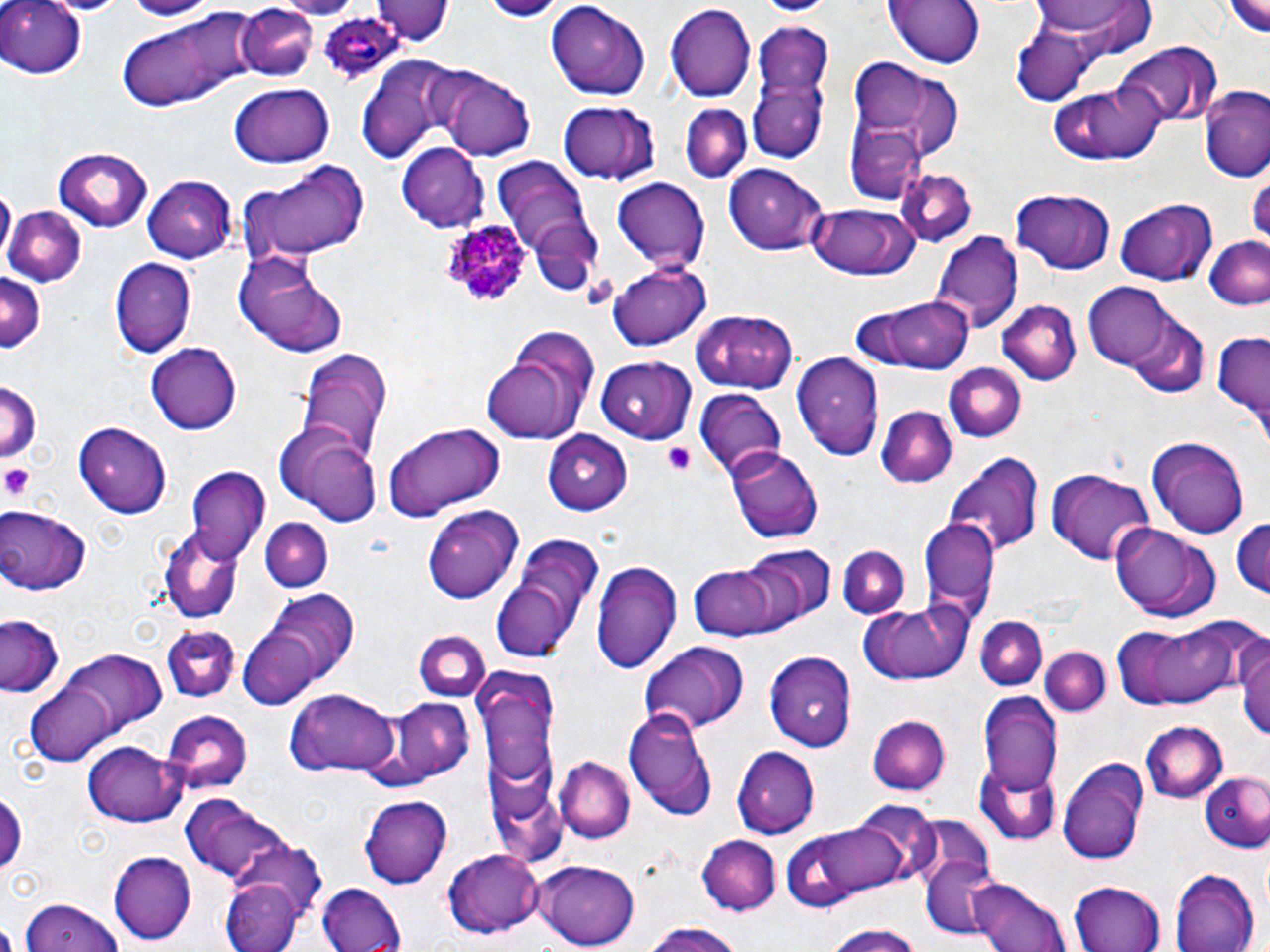

Summary:
  - Coordinate format: approximate bounding boxes as named x1/y1/x2/y2 corners in pixels
  - Platelet locations: (x1=664, y1=444, x2=696, y2=476), (x1=1, y1=464, x2=38, y2=502)
  - Plasmodium ovale-infected red blood cell locations: (x1=319, y1=8, x2=403, y2=81), (x1=440, y1=218, x2=529, y2=307)
  - Uninfected red blood cell locations: (x1=122, y1=0, x2=215, y2=20), (x1=281, y1=0, x2=357, y2=16), (x1=378, y1=0, x2=452, y2=46), (x1=757, y1=0, x2=835, y2=17), (x1=887, y1=0, x2=983, y2=68), (x1=1222, y1=0, x2=1270, y2=38), (x1=0, y1=1, x2=90, y2=79), (x1=46, y1=1, x2=129, y2=15), (x1=1030, y1=1, x2=1155, y2=49), (x1=543, y1=2, x2=650, y2=102), (x1=665, y1=3, x2=754, y2=102), (x1=234, y1=5, x2=321, y2=81), (x1=119, y1=14, x2=263, y2=111), (x1=747, y1=19, x2=833, y2=164), (x1=1009, y1=28, x2=1097, y2=105), (x1=1114, y1=43, x2=1221, y2=126), (x1=354, y1=55, x2=466, y2=164), (x1=849, y1=59, x2=967, y2=160), (x1=442, y1=71, x2=534, y2=161), (x1=1052, y1=80, x2=1168, y2=166), (x1=229, y1=83, x2=335, y2=169), (x1=1202, y1=91, x2=1270, y2=181), (x1=555, y1=101, x2=663, y2=187), (x1=680, y1=104, x2=751, y2=183), (x1=847, y1=125, x2=923, y2=204), (x1=396, y1=141, x2=489, y2=229), (x1=53, y1=146, x2=153, y2=230), (x1=493, y1=157, x2=597, y2=268), (x1=239, y1=160, x2=371, y2=263), (x1=726, y1=165, x2=830, y2=257), (x1=896, y1=169, x2=975, y2=247), (x1=143, y1=176, x2=238, y2=261), (x1=610, y1=177, x2=709, y2=275), (x1=0, y1=185, x2=14, y2=264), (x1=1012, y1=191, x2=1115, y2=274), (x1=1117, y1=200, x2=1216, y2=283), (x1=807, y1=203, x2=920, y2=282), (x1=4, y1=205, x2=84, y2=289), (x1=528, y1=221, x2=601, y2=296), (x1=927, y1=230, x2=1023, y2=334), (x1=1203, y1=235, x2=1270, y2=314), (x1=232, y1=250, x2=350, y2=359), (x1=108, y1=256, x2=196, y2=359), (x1=606, y1=262, x2=712, y2=351), (x1=0, y1=274, x2=43, y2=355), (x1=1084, y1=283, x2=1176, y2=370), (x1=846, y1=295, x2=976, y2=376), (x1=996, y1=300, x2=1080, y2=387), (x1=695, y1=308, x2=800, y2=393), (x1=1127, y1=310, x2=1209, y2=398), (x1=1210, y1=331, x2=1269, y2=433), (x1=146, y1=343, x2=242, y2=434), (x1=292, y1=348, x2=396, y2=464), (x1=483, y1=348, x2=591, y2=444), (x1=789, y1=353, x2=885, y2=460), (x1=596, y1=356, x2=694, y2=443), (x1=945, y1=363, x2=1027, y2=444), (x1=0, y1=379, x2=41, y2=468), (x1=695, y1=390, x2=785, y2=484), (x1=875, y1=407, x2=955, y2=488), (x1=383, y1=422, x2=505, y2=519), (x1=73, y1=423, x2=170, y2=516), (x1=274, y1=425, x2=382, y2=527), (x1=545, y1=431, x2=632, y2=515), (x1=1147, y1=435, x2=1249, y2=541), (x1=727, y1=449, x2=822, y2=543), (x1=943, y1=452, x2=1042, y2=556), (x1=186, y1=468, x2=271, y2=567), (x1=1046, y1=469, x2=1153, y2=564), (x1=421, y1=505, x2=525, y2=604), (x1=0, y1=506, x2=91, y2=594), (x1=1231, y1=515, x2=1270, y2=603), (x1=917, y1=516, x2=999, y2=623), (x1=260, y1=517, x2=332, y2=591), (x1=1110, y1=523, x2=1220, y2=623), (x1=488, y1=531, x2=600, y2=662), (x1=158, y1=532, x2=243, y2=623), (x1=838, y1=542, x2=911, y2=619), (x1=739, y1=543, x2=834, y2=629), (x1=590, y1=557, x2=684, y2=673), (x1=688, y1=564, x2=784, y2=640), (x1=257, y1=589, x2=360, y2=690), (x1=856, y1=601, x2=971, y2=685), (x1=1114, y1=613, x2=1262, y2=711), (x1=2, y1=614, x2=64, y2=699), (x1=976, y1=617, x2=1047, y2=692), (x1=160, y1=623, x2=239, y2=701), (x1=413, y1=629, x2=490, y2=702), (x1=1238, y1=629, x2=1270, y2=746), (x1=237, y1=630, x2=322, y2=709), (x1=639, y1=641, x2=751, y2=735), (x1=1041, y1=648, x2=1110, y2=717), (x1=36, y1=650, x2=168, y2=748), (x1=766, y1=651, x2=857, y2=750), (x1=476, y1=667, x2=563, y2=809), (x1=21, y1=677, x2=127, y2=768), (x1=284, y1=689, x2=403, y2=778), (x1=981, y1=692, x2=1062, y2=795), (x1=387, y1=697, x2=472, y2=784), (x1=624, y1=705, x2=719, y2=820), (x1=162, y1=710, x2=251, y2=794), (x1=869, y1=716, x2=950, y2=797), (x1=1140, y1=720, x2=1228, y2=802), (x1=81, y1=742, x2=185, y2=827), (x1=730, y1=745, x2=819, y2=837), (x1=554, y1=755, x2=635, y2=845), (x1=1058, y1=756, x2=1151, y2=864), (x1=976, y1=765, x2=1062, y2=845), (x1=1203, y1=772, x2=1270, y2=854), (x1=0, y1=789, x2=24, y2=880), (x1=179, y1=794, x2=297, y2=887), (x1=357, y1=795, x2=453, y2=888), (x1=852, y1=804, x2=941, y2=889), (x1=777, y1=816, x2=908, y2=913), (x1=697, y1=836, x2=781, y2=914), (x1=229, y1=843, x2=328, y2=926), (x1=107, y1=850, x2=198, y2=944), (x1=441, y1=851, x2=547, y2=939), (x1=917, y1=857, x2=1011, y2=940), (x1=533, y1=861, x2=640, y2=948), (x1=1169, y1=869, x2=1259, y2=952), (x1=219, y1=876, x2=305, y2=952), (x1=965, y1=876, x2=1072, y2=952), (x1=314, y1=880, x2=408, y2=950), (x1=1069, y1=882, x2=1166, y2=952), (x1=17, y1=895, x2=123, y2=952), (x1=639, y1=921, x2=746, y2=952), (x1=820, y1=922, x2=930, y2=952)
  - Slide-level diagnosis: Plasmodium ovale
  - Magnification: 1000x
  - Modality: light microscopy
  - Preparation: thin blood smear
  - Field of view: one of a larger specimen
  - Image size: 1270×952 pixels
  - Stain: May-Grünwald-Giemsa